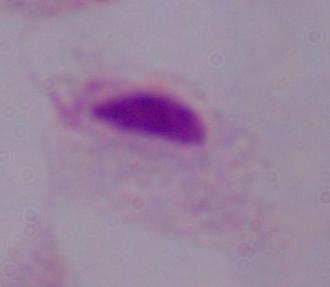 A trichomonad is shown. Micrograph. Captured at 1000x magnification.